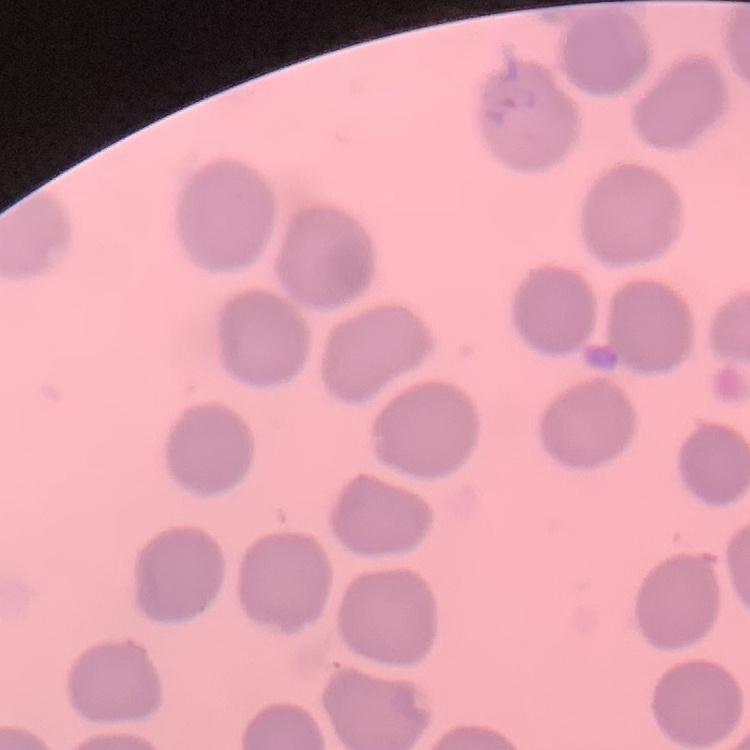
The erythrocytes show no rouleaux formation. Field's or Giemsa stain. Square crop of a larger photomicrograph. Thin blood film.